Describe the morphology of the erythrocytes.
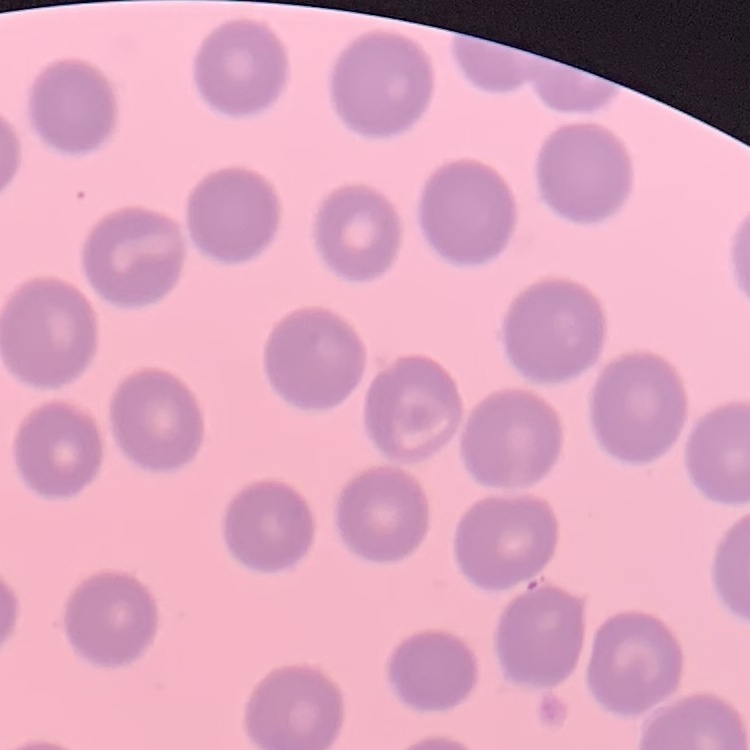
No rouleaux formation.

Summary:
  - Preparation: thin blood smear
  - Image type: one tile cut from a larger photomicrograph
  - Stain: Field's or Giemsa